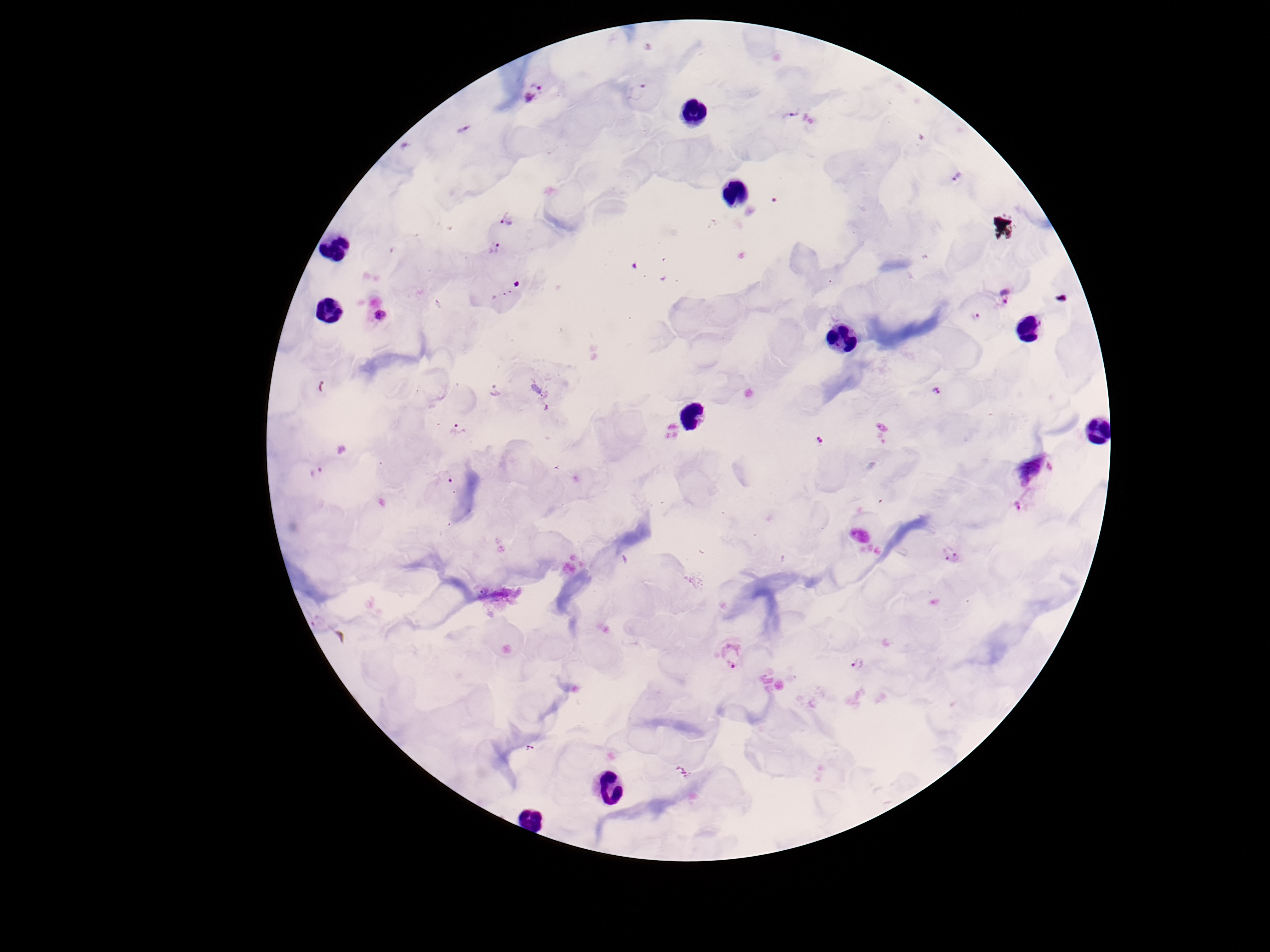
patient malaria status = infected
Plasmodium parasite locations = approximate centers as {x, y} in pixels: {636, 90}, {531, 94}, {795, 110}, {463, 130}, {957, 177}, {508, 219}, {494, 249}, {1005, 295}, {381, 315}, {976, 318}, {495, 390}, {936, 392}, {458, 428}, {817, 442}, {318, 473}, {447, 476}, {1026, 499}, {951, 556}, {319, 624}, {732, 653}, {857, 664}, {530, 750}
magnification = 100x
field of view = one from this slide
stain = Giemsa
image size = 1270×952 pixels
capture = smartphone camera through the microscope eyepiece
preparation = thick blood film